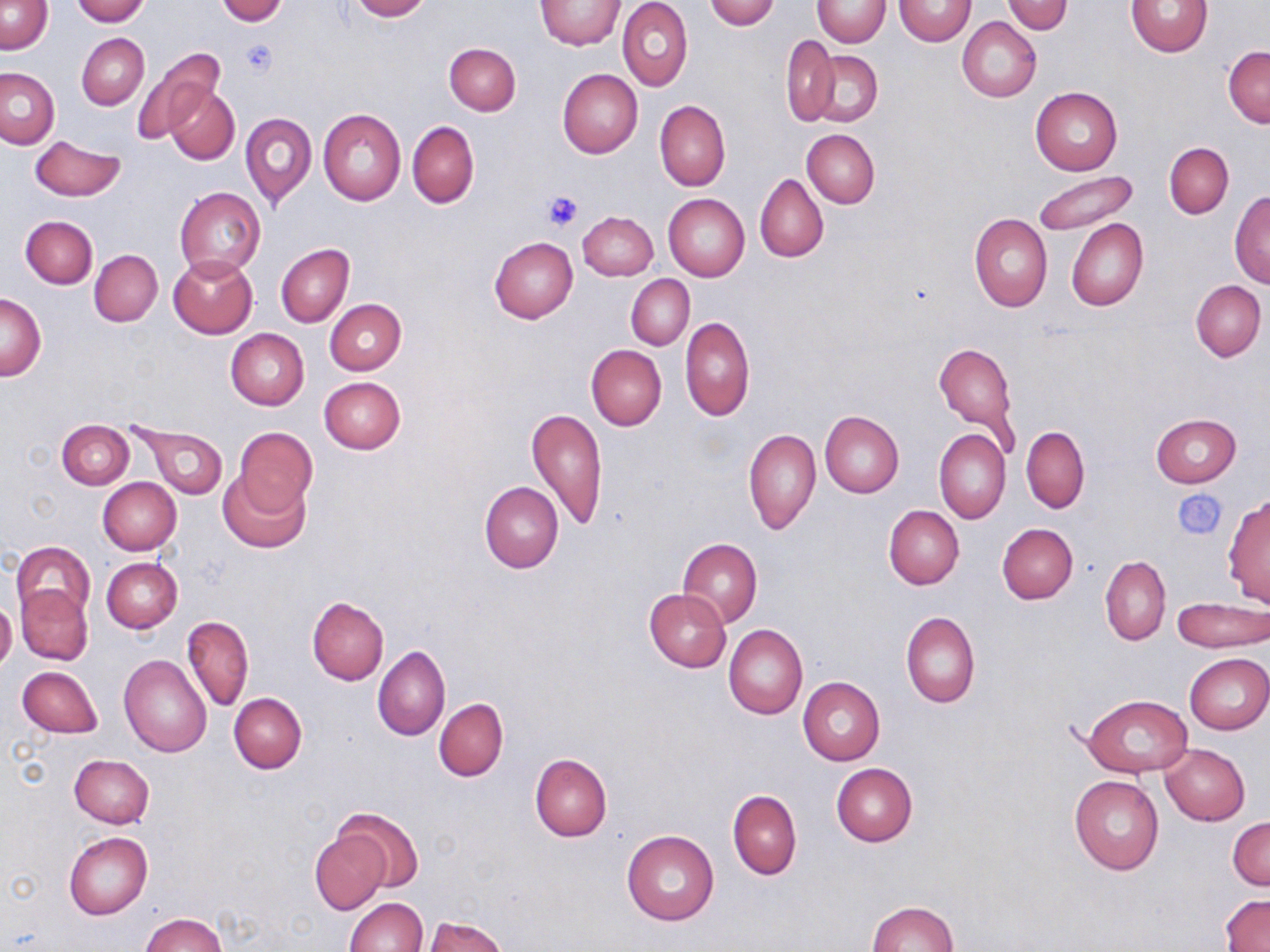
slide-level diagnosis = negative for blood parasites
platelet locations = approximate bounding boxes as [x1, y1, x2, y2] in pixels: [239, 38, 278, 77], [543, 191, 584, 232], [1176, 490, 1224, 538]
uninfected red blood cell locations = approximate bounding boxes as [x1, y1, x2, y2] in pixels: [72, 0, 150, 25], [347, 0, 430, 21], [618, 0, 693, 91], [707, 0, 778, 29], [812, 0, 889, 47], [894, 0, 975, 46], [0, 1, 53, 55], [217, 1, 287, 24], [536, 1, 624, 49], [1002, 1, 1072, 35], [1126, 1, 1211, 58], [958, 16, 1041, 103], [77, 33, 149, 110], [782, 35, 841, 127], [445, 43, 520, 116], [1224, 45, 1269, 128], [130, 46, 223, 146], [806, 51, 882, 128], [0, 67, 60, 149], [558, 69, 642, 157], [165, 83, 238, 166], [1030, 86, 1123, 175], [655, 100, 731, 192], [317, 108, 406, 205], [242, 114, 317, 208], [407, 121, 479, 208], [802, 130, 879, 208], [31, 135, 126, 201], [1164, 143, 1233, 218], [1033, 169, 1140, 236], [755, 173, 827, 262], [174, 186, 265, 278], [1229, 191, 1270, 287], [663, 194, 749, 282], [577, 211, 658, 281], [970, 213, 1052, 312], [21, 216, 97, 288], [1067, 218, 1147, 312], [489, 237, 578, 323], [275, 244, 354, 328], [89, 250, 162, 326], [168, 255, 258, 338], [627, 275, 694, 349], [1191, 280, 1266, 362], [1, 294, 46, 380], [324, 300, 406, 375], [680, 316, 755, 421], [225, 329, 308, 410], [932, 340, 1019, 442], [586, 344, 667, 430], [319, 377, 406, 453], [527, 407, 608, 531], [820, 411, 903, 497], [1150, 413, 1241, 488], [56, 419, 134, 490], [132, 422, 228, 500], [233, 427, 318, 516], [1020, 427, 1089, 513], [743, 429, 821, 534], [934, 429, 1010, 524], [218, 471, 312, 553], [98, 477, 181, 555], [479, 481, 562, 573], [1223, 493, 1270, 607], [884, 505, 964, 589], [996, 523, 1078, 604], [678, 538, 762, 628], [12, 542, 94, 619], [1099, 556, 1171, 645], [101, 558, 182, 633], [17, 584, 93, 665], [644, 589, 731, 671], [307, 596, 388, 685], [1172, 598, 1268, 652], [0, 600, 16, 671], [901, 612, 981, 708], [183, 615, 254, 712], [724, 623, 807, 719], [373, 646, 450, 741], [119, 654, 211, 756], [1185, 654, 1269, 734], [17, 666, 102, 738], [797, 677, 886, 765], [229, 693, 307, 773], [1081, 693, 1194, 777], [433, 698, 508, 781], [1160, 744, 1250, 825], [529, 753, 611, 842], [69, 754, 155, 828], [831, 763, 918, 846], [1069, 776, 1164, 876], [727, 790, 802, 880], [333, 807, 425, 894], [1228, 817, 1269, 890], [621, 830, 719, 926], [310, 831, 389, 914], [64, 832, 153, 919], [1220, 893, 1270, 951], [344, 897, 426, 951], [867, 900, 959, 952], [140, 913, 228, 952], [423, 915, 507, 952]
field of view = one of a larger specimen
modality = light microscopy
stain = May-Grünwald-Giemsa
preparation = thin blood smear
magnification = 1000x
image size = 1270×952 pixels